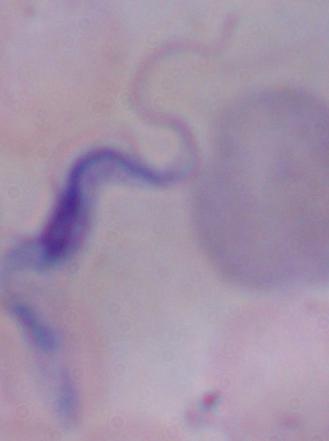
Summary:
  - Modality: photomicrograph
  - Magnification: 1000x
  - Identification: trypanosome